Classify this cell by malaria status.
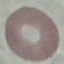

It is uninfected.

{
  "preparation": "thin blood film",
  "stain": "Giemsa",
  "image_type": "automatically extracted cell patch, resized to 64 × 64 pixels",
  "capture": "smartphone through the microscope eyepiece"
}